Locate every blood parasite and identify its species.
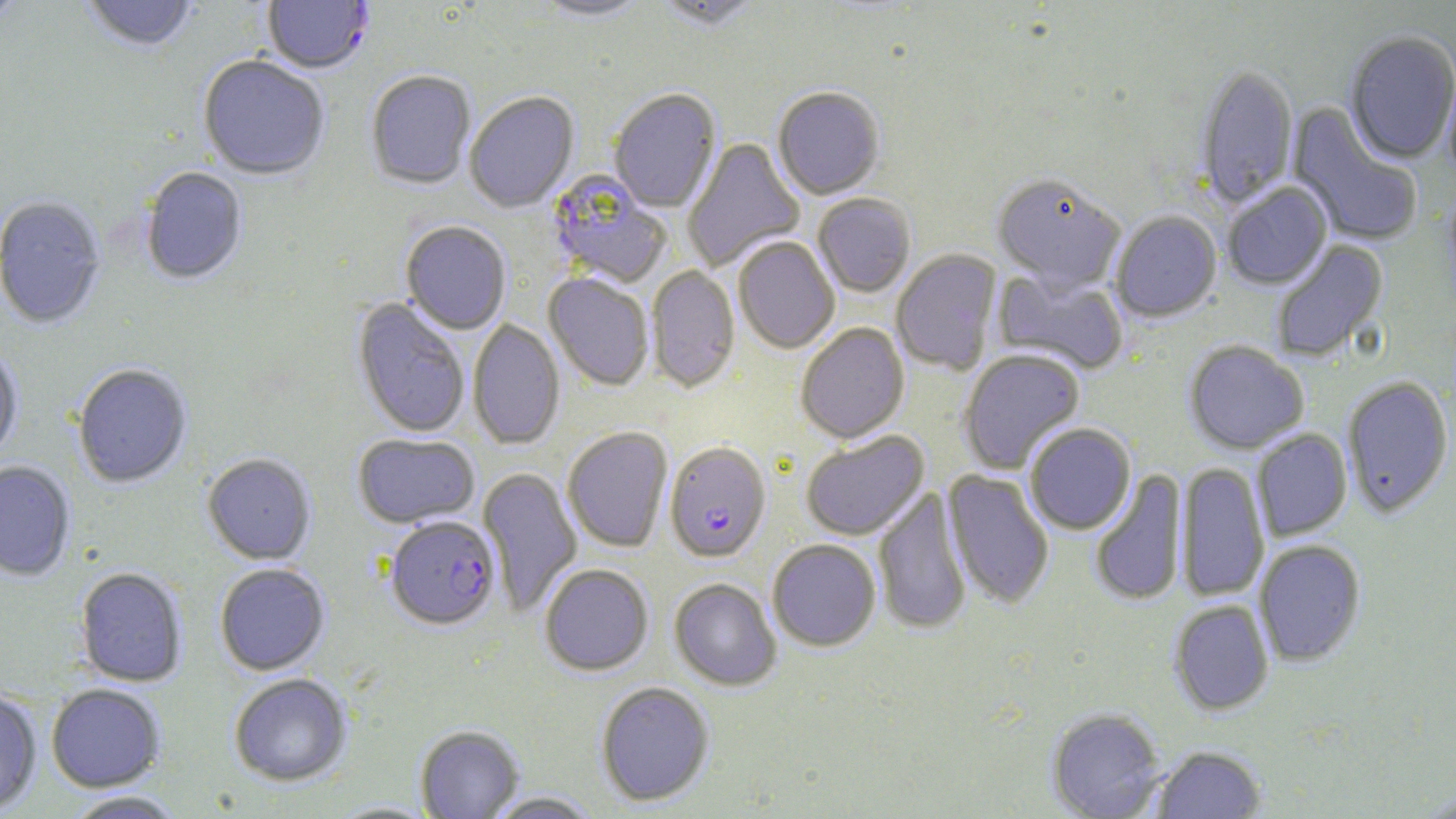
Approximate bounding boxes as (x1,y1)-(x2,y2) corner pairs in pixels.
Plasmodium falciparum-infected red blood cells: (262,0)-(374,76), (664,442)-(770,563), (385,515)-(500,631).
No Plasmodium ovale, Plasmodium malariae, Plasmodium vivax, Babesia divergens, or Trypanosoma brucei observed.

Summary:
  - Uninfected red blood cell locations: (0,0)-(26,25), (80,0)-(200,54), (532,0)-(652,22), (656,0)-(763,33), (1344,32)-(1456,166), (197,57)-(329,181), (1195,66)-(1298,209), (1442,67)-(1456,184), (365,71)-(476,190), (608,89)-(721,214), (772,89)-(885,202), (464,92)-(579,213), (1286,103)-(1423,247), (682,138)-(805,272), (140,168)-(248,286), (546,170)-(671,288), (991,175)-(1125,292), (1222,183)-(1332,291), (812,194)-(916,298), (0,197)-(106,329), (1110,211)-(1222,323), (401,221)-(511,335), (733,236)-(840,354), (1271,239)-(1389,362), (891,249)-(1002,375), (647,266)-(740,392), (993,268)-(1129,375), (544,273)-(654,390), (353,298)-(470,439), (468,319)-(564,450), (795,323)-(909,443), (1184,341)-(1309,454), (0,346)-(23,464), (958,349)-(1085,474), (73,364)-(192,488), (1342,376)-(1454,518), (1024,423)-(1136,535), (562,426)-(673,552), (1252,429)-(1351,541), (800,431)-(930,541), (353,433)-(479,529), (202,454)-(316,565), (0,461)-(75,580), (1176,462)-(1269,602), (477,467)-(582,616), (943,469)-(1054,610), (1090,469)-(1188,607), (872,487)-(972,636), (767,539)-(881,651), (1254,540)-(1366,666), (214,563)-(330,675), (539,563)-(654,676), (75,567)-(188,687), (669,578)-(781,691), (1169,599)-(1274,715), (229,674)-(352,787), (595,681)-(715,807), (46,684)-(166,792), (0,691)-(42,815), (1047,708)-(1165,819), (415,724)-(524,819), (1151,745)-(1266,818), (1417,790)-(1456,818), (64,791)-(187,818), (485,791)-(602,818), (325,801)-(443,818)
  - Slide-level diagnosis: Plasmodium falciparum
  - Image size: 1456×819 pixels
  - Modality: optical microscopy
  - Stain: May-Grünwald-Giemsa
  - Field of view: one of a larger specimen
  - Magnification: 1000x
  - Preparation: thin blood smear